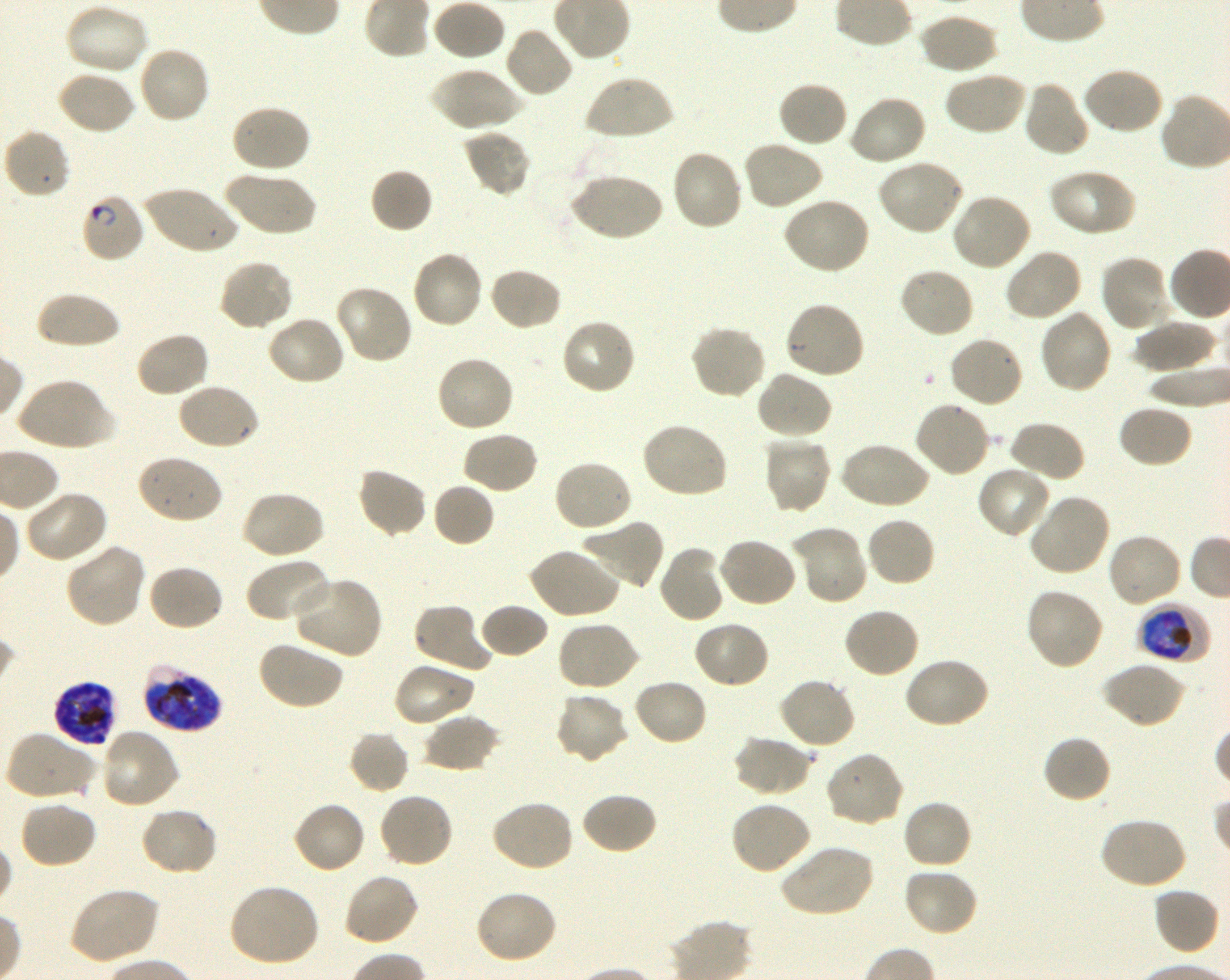

Approximate bounding boxes as (x1, y1, x2, y2) in pixels. Not every red blood cell is marked. A life-cycle stage — or a range of stages, where the recorded stages span more than one — follows each staged infected red blood cell. Locations of infected red blood cells: (80, 192, 146, 263) ring; (1137, 603, 1211, 664) trophozoite; (142, 663, 222, 733) late trophozoite to late schizont; (52, 681, 117, 747) schizont. Locations of uninfected red blood cells: (431, 0, 506, 62), (63, 3, 150, 76), (917, 12, 998, 75), (503, 26, 574, 99), (137, 44, 211, 124), (430, 66, 522, 132), (1080, 66, 1164, 136), (943, 70, 1027, 136), (56, 71, 137, 136), (583, 73, 674, 142), (777, 80, 850, 148), (1022, 80, 1090, 158), (847, 94, 927, 167), (230, 103, 312, 174), (3, 127, 72, 199), (463, 128, 531, 197), (741, 141, 825, 211), (670, 149, 744, 232), (875, 159, 965, 237), (1048, 168, 1137, 237), (223, 169, 317, 238), (370, 169, 433, 235), (569, 172, 663, 242), (143, 184, 239, 255), (951, 191, 1033, 272), (780, 197, 871, 276), (1003, 248, 1083, 322), (410, 249, 484, 330), (1099, 254, 1172, 334), (218, 259, 295, 333), (487, 266, 563, 332), (897, 266, 975, 339), (334, 283, 414, 364), (34, 292, 122, 349), (783, 300, 867, 380), (1037, 308, 1113, 395), (266, 314, 347, 386), (560, 317, 637, 396), (1132, 319, 1217, 373), (689, 325, 767, 399), (134, 331, 210, 399), (948, 335, 1024, 410), (435, 355, 515, 434), (755, 370, 833, 440), (15, 377, 114, 452), (176, 382, 260, 451), (914, 400, 991, 478), (1116, 404, 1193, 469), (1007, 420, 1085, 483), (639, 422, 729, 500), (460, 431, 539, 495), (762, 435, 833, 514), (838, 441, 930, 510), (135, 454, 223, 525), (552, 458, 633, 532), (976, 465, 1053, 540), (356, 466, 428, 539), (432, 482, 495, 548), (22, 489, 109, 564), (240, 489, 325, 561), (1028, 493, 1112, 577), (864, 516, 936, 588), (581, 519, 665, 591), (792, 526, 868, 606), (1106, 532, 1183, 608), (717, 537, 798, 609), (64, 542, 146, 629), (657, 545, 726, 624), (527, 546, 620, 619), (246, 557, 333, 625), (146, 564, 224, 632), (289, 575, 383, 660), (1024, 587, 1104, 671), (413, 603, 493, 674), (479, 603, 548, 659), (842, 606, 921, 679), (691, 620, 770, 689), (556, 621, 640, 692), (257, 640, 343, 711), (902, 656, 990, 729), (1099, 661, 1185, 729), (392, 662, 476, 727), (777, 676, 856, 750), (633, 678, 709, 747), (554, 692, 631, 765), (423, 713, 501, 773), (101, 727, 181, 809), (347, 729, 409, 794), (4, 731, 97, 801), (733, 735, 813, 798), (1041, 735, 1112, 804), (824, 750, 906, 827), (378, 792, 455, 868), (581, 792, 658, 855), (901, 798, 973, 870), (490, 799, 575, 872), (19, 800, 98, 870), (291, 800, 366, 875), (729, 800, 811, 874), (139, 806, 219, 877), (1098, 817, 1186, 891), (777, 844, 874, 918), (902, 866, 979, 938), (342, 872, 420, 946), (227, 883, 321, 968), (67, 886, 159, 965), (1152, 886, 1221, 956), (473, 889, 558, 964). Life-cycle stages observed: ring, trophozoite, schizont. Donor blood group O+. One field from this slide. Shaking in-vitro culture of Plasmodium falciparum strain 3D7. Image is 1230×980 pixels. Thin blood film. 100x oil-immersion objective, numerical aperture 1.30. Giemsa stain.